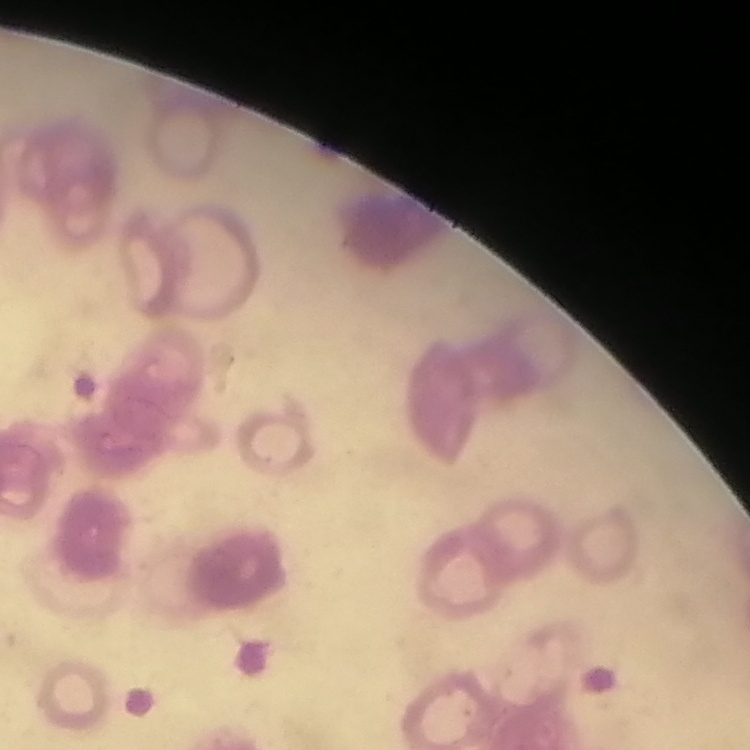

{
  "red_blood_cell_morphology": "rouleaux formation",
  "preparation": "thin blood film",
  "image_type": "square crop of a larger photomicrograph",
  "stain": "Field's or Giemsa"
}